Describe the morphology of the erythrocytes.
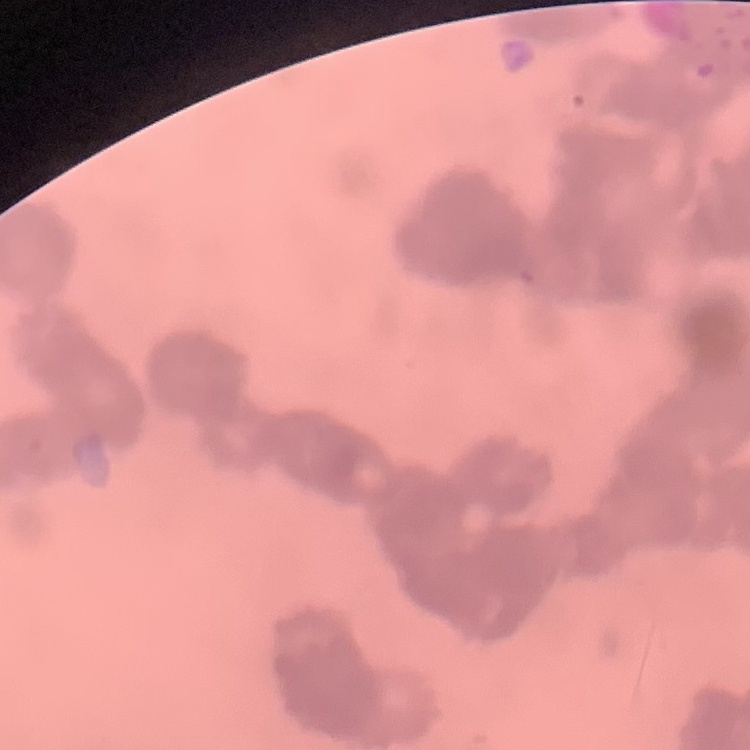

They show rouleaux formation.

{
  "preparation": "thin blood film",
  "image_type": "square crop of a larger photomicrograph",
  "stain": "Field's or Giemsa"
}